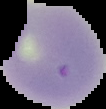

image size = 106×109 pixels
malaria status = uninfected
preparation = thin blood smear
image type = cell region segmented out of the field of view; surrounding area masked to black